State which parasite is depicted.
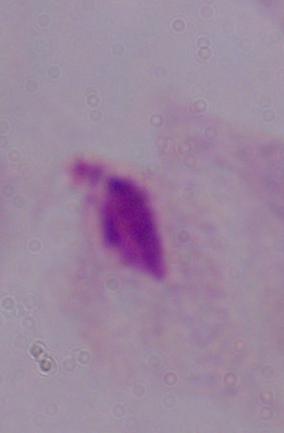
This is a trichomonad.

magnification: 1000x
modality: micrograph